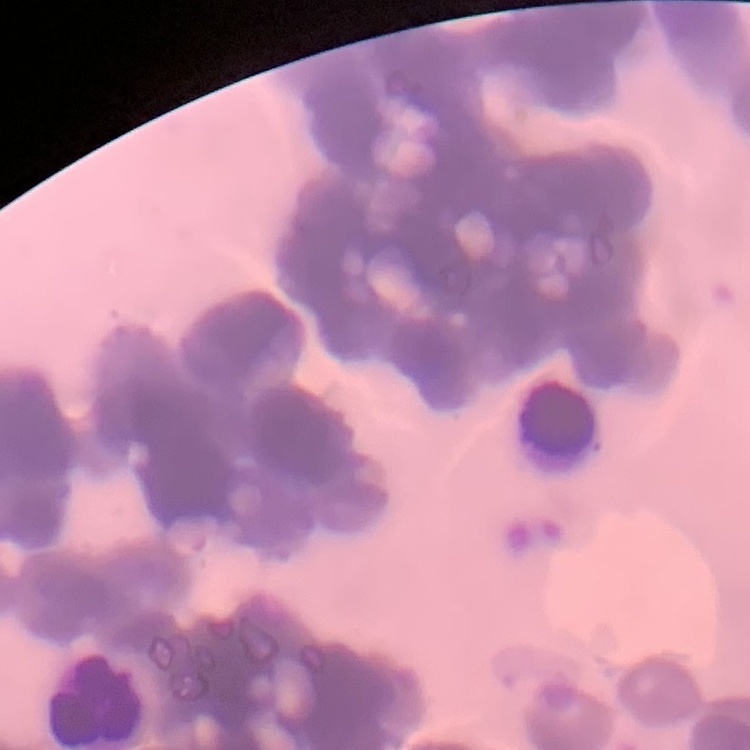
{
  "erythrocyte_morphology": "rouleaux formation",
  "preparation": "thin blood smear",
  "stain": "Field's or Giemsa",
  "image_type": "square crop of a larger photomicrograph"
}